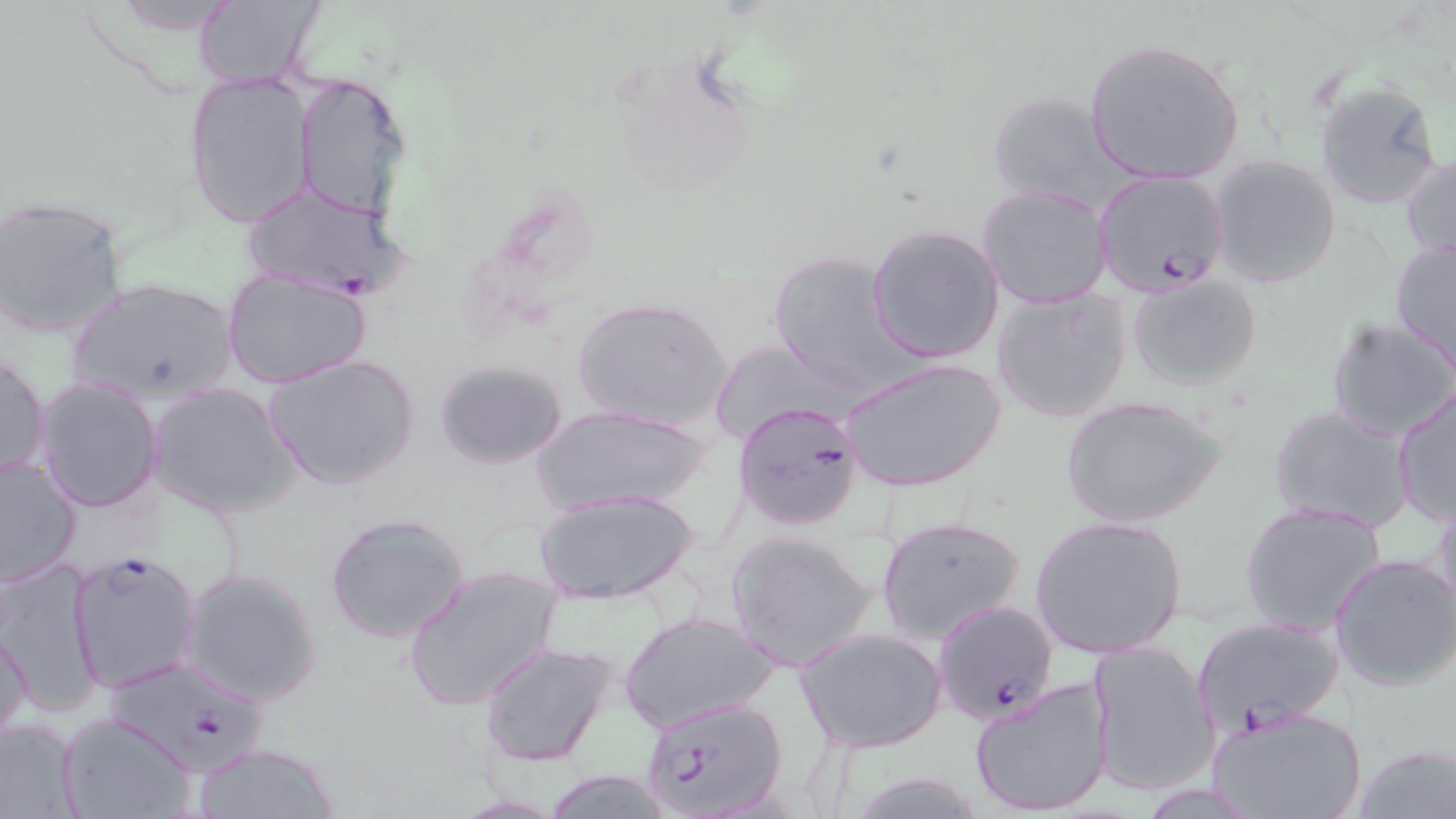
slide-level diagnosis = Plasmodium falciparum
field of view = single
image size = 1456×819 pixels
uninfected red blood cell locations = approximate bounding boxes as (x1, y1, x2, y2) in pixels: (187, 2, 324, 88), (1083, 39, 1246, 186), (605, 52, 759, 203), (183, 73, 315, 228), (292, 75, 410, 221), (1314, 79, 1447, 211), (984, 89, 1130, 213), (1401, 153, 1456, 267), (1208, 155, 1342, 289), (977, 185, 1112, 308), (0, 197, 129, 338), (867, 224, 1006, 364), (1390, 237, 1456, 373), (768, 248, 907, 392), (221, 267, 371, 390), (1125, 273, 1262, 390), (64, 277, 241, 408), (990, 287, 1134, 423), (571, 296, 735, 433), (1326, 316, 1456, 442), (710, 339, 840, 444), (1, 351, 49, 484), (263, 355, 419, 490), (838, 356, 1005, 494), (432, 359, 569, 470), (34, 377, 165, 513), (148, 381, 301, 519), (1389, 383, 1456, 527), (1061, 394, 1225, 527), (531, 403, 713, 515), (1267, 406, 1414, 534), (0, 454, 82, 589), (535, 488, 699, 607), (1431, 489, 1456, 618), (1238, 500, 1389, 636), (324, 511, 473, 646), (877, 514, 1026, 645), (1029, 514, 1189, 660), (725, 529, 879, 670), (1329, 554, 1456, 690), (1, 559, 103, 716), (402, 565, 562, 712), (178, 566, 323, 705), (618, 609, 780, 735), (1, 624, 32, 748), (795, 627, 949, 754), (1085, 640, 1219, 797), (478, 641, 619, 767), (967, 674, 1116, 817), (1205, 704, 1368, 819), (59, 714, 195, 819), (0, 717, 83, 817), (191, 743, 340, 819), (1350, 743, 1456, 819), (536, 768, 675, 819), (838, 768, 994, 819)
modality = light microscopy
preparation = thin blood smear
magnification = 1000x
stain = May-Grünwald-Giemsa
Plasmodium falciparum-infected red blood cell locations = approximate bounding boxes as (x1, y1, x2, y2) in pixels: (1092, 169, 1230, 298), (238, 183, 403, 299), (733, 399, 864, 531), (67, 548, 203, 693), (925, 602, 1052, 729), (1193, 616, 1345, 731), (105, 657, 273, 776), (639, 697, 790, 819)